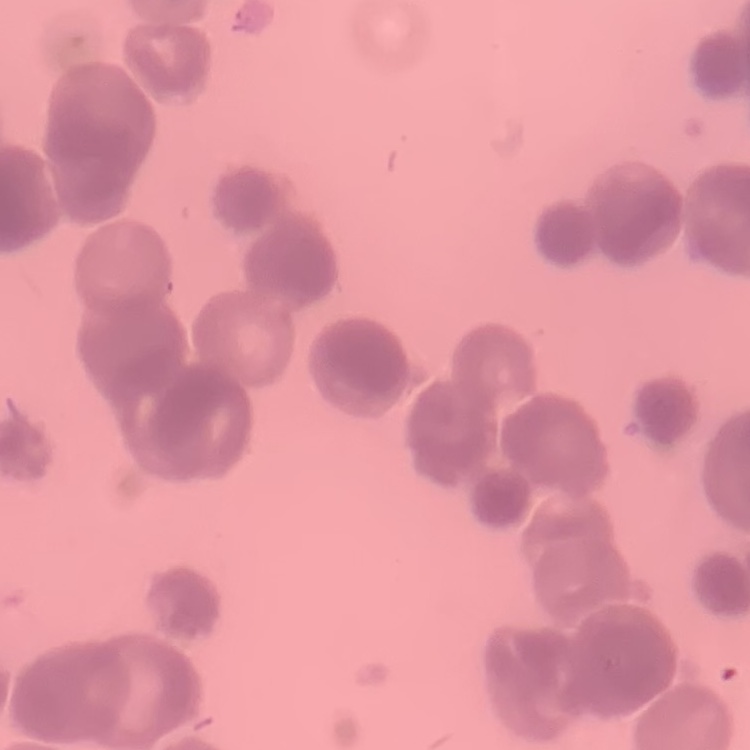 The red blood cells exhibit rouleaux formation. Square crop of a larger photomicrograph. Thin peripheral smear. Field's or Giemsa stain.